Locate every malaria parasite and every leukocyte.
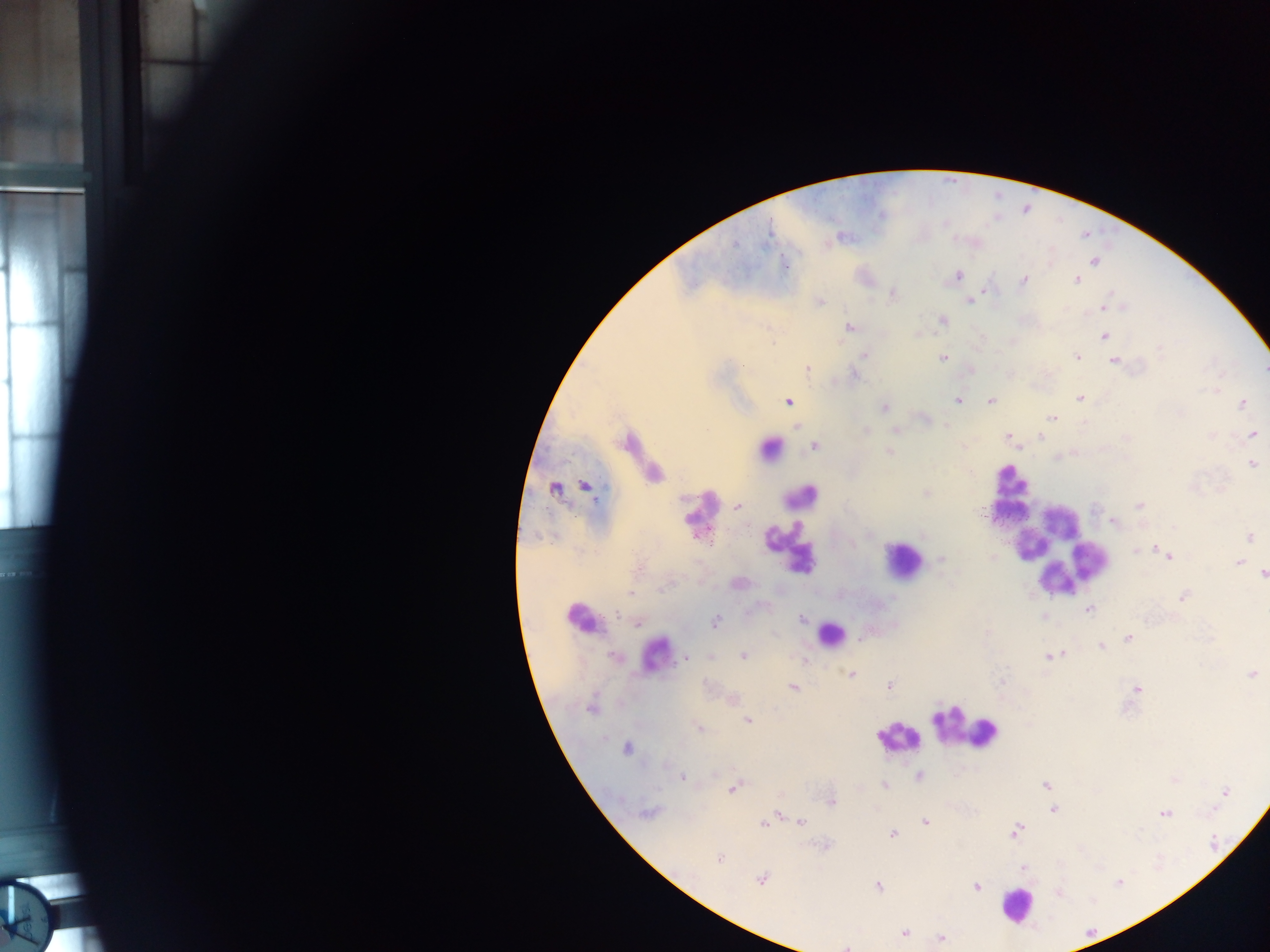
Approximate centers as [x, y] in pixels.
Malaria parasites: [770, 234], [840, 236], [1093, 261], [783, 264], [958, 276], [1075, 279], [1024, 280], [893, 295], [969, 299], [1108, 303], [1108, 307], [942, 320], [849, 327], [1104, 338], [1161, 350], [864, 354], [1075, 357], [942, 358], [1114, 360], [807, 370], [1219, 388], [1216, 391], [1079, 399], [957, 400], [789, 402], [990, 402], [1242, 404], [882, 407], [1053, 418], [1082, 424], [797, 426], [865, 431], [896, 431], [1251, 435], [1007, 436], [1041, 438], [814, 446], [1017, 448], [888, 452], [1252, 464], [969, 471], [925, 493], [1139, 505], [736, 506], [983, 512], [1115, 522], [1250, 536], [536, 537], [1153, 549], [1134, 550], [993, 557], [1170, 558], [940, 559], [1239, 563], [1261, 574], [664, 586], [630, 593], [1182, 596], [1088, 609], [618, 614], [1044, 616], [802, 619], [638, 622], [716, 623], [866, 634], [1127, 639], [1100, 646], [1062, 654], [711, 656], [743, 656], [1049, 656], [686, 659], [805, 661], [852, 674], [1251, 674], [890, 685], [794, 687], [1137, 688], [749, 720], [698, 727], [627, 750], [683, 777], [1044, 785], [885, 786], [732, 789], [1226, 792], [1214, 808], [1053, 809], [650, 812], [643, 813], [1166, 815], [800, 820], [925, 821], [763, 823], [1016, 831], [893, 833], [1140, 834], [721, 860], [761, 880], [1118, 884], [977, 886], [879, 887], [906, 932], [942, 939], [846, 947].
Leukocytes: [769, 448], [1014, 493], [794, 535], [1061, 552], [898, 557], [578, 618], [833, 631], [964, 731], [895, 737], [1011, 901].

Thick blood film. Photographed through a microscope with a mobile-phone camera. Image is 1270×952 pixels. One field of view. Sample from Ghana.